Locate every blood parasite and identify its species.
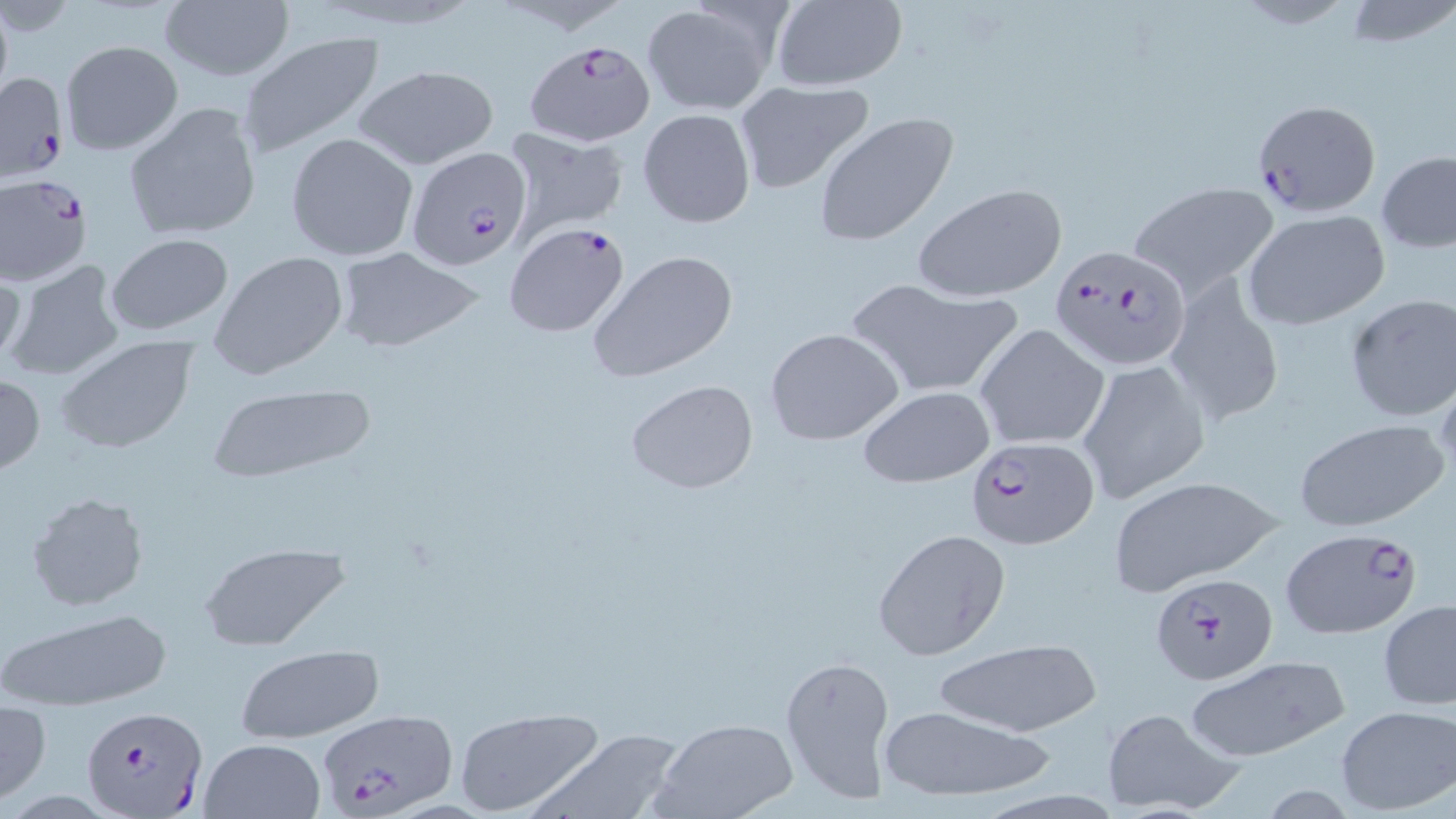

Approximate bounding boxes as (x1,y1)-(x2,y2) corner pairs in pixels.
Plasmodium falciparum-infected red blood cells (subset): (526,39)-(655,146), (0,71)-(68,183), (1252,99)-(1382,217), (407,144)-(532,272), (0,172)-(94,283), (505,221)-(630,337), (1050,245)-(1191,370), (965,435)-(1098,549), (1150,570)-(1279,684), (79,706)-(206,818), (314,707)-(458,816).
No Plasmodium ovale, Plasmodium malariae, Plasmodium vivax, Babesia divergens, or Trypanosoma brucei observed.

Uninfected red blood cell locations (subset): (1340,0)-(1456,50), (158,1)-(294,84), (769,1)-(908,92), (641,3)-(777,115), (237,31)-(384,157), (59,40)-(183,156), (351,64)-(500,170), (734,81)-(874,195), (123,102)-(261,242), (638,107)-(755,229), (812,112)-(958,249), (503,128)-(627,239), (286,131)-(419,261), (1376,149)-(1456,253), (1130,180)-(1279,296), (912,182)-(1067,303), (1242,208)-(1391,330), (102,234)-(234,337), (331,246)-(484,353), (588,250)-(739,382), (210,252)-(350,377), (3,258)-(126,383), (0,260)-(27,372), (1165,275)-(1282,424), (842,277)-(1025,399), (1343,294)-(1455,423), (975,323)-(1109,452), (765,327)-(904,446), (55,337)-(198,455), (1078,359)-(1211,502), (0,372)-(45,476), (626,380)-(759,494), (205,382)-(377,482), (860,387)-(995,488), (1294,419)-(1449,533), (1104,476)-(1283,592), (26,491)-(151,612), (873,529)-(1011,660), (196,544)-(350,651), (1378,601)-(1456,710), (0,609)-(172,709), (927,637)-(1106,740), (236,646)-(385,744), (780,652)-(897,807), (1185,655)-(1350,759), (0,701)-(50,802), (877,705)-(1056,804), (1334,705)-(1455,815), (452,706)-(604,817), (1101,707)-(1242,816), (649,718)-(798,819), (527,727)-(687,819), (198,737)-(327,819). Slide-level diagnosis: Plasmodium falciparum. Light microscopy. May-Grünwald-Giemsa stain. Captured at 1000x magnification. Image is 1456×819 pixels. Thin blood smear. Single field of view.